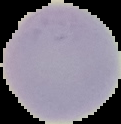
Summary:
  - Image type: segmented cell region on a black background
  - Result: no Plasmodium parasites detected
  - Image size: 121×124 pixels
  - Preparation: thin blood film